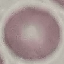

Malaria status: uninfected. Acquired by smartphone through the microscope eyepiece. Cell patch, automatically extracted from a larger field of view and resized to 64 × 64 pixels. Thin blood film. Giemsa-stained preparation.